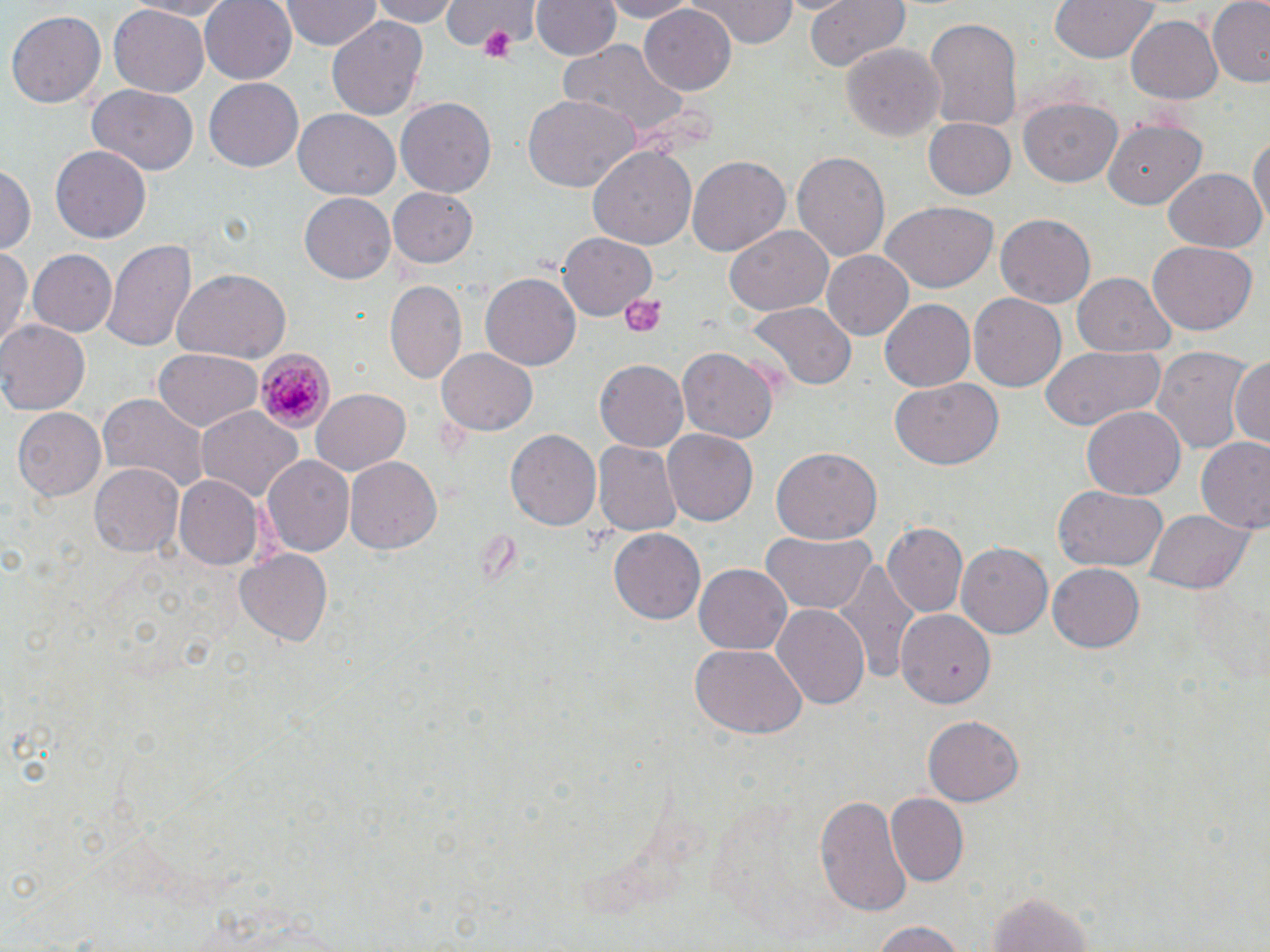
Approximate bounding boxes as (x1,y1)-(x2,y2) corner pairs in pixels. Platelet locations: (477,24)-(518,62), (621,292)-(664,335). Plasmodium malariae-infected red blood cell locations: (258,348)-(334,433). Uninfected red blood cell locations: (125,0)-(241,19), (199,0)-(297,83), (279,0)-(385,53), (369,0)-(456,27), (443,0)-(540,60), (598,0)-(697,21), (689,0)-(795,46), (802,0)-(911,72), (1049,0)-(1161,61), (1206,0)-(1270,85), (532,1)-(619,61), (640,4)-(736,94), (107,7)-(210,95), (6,9)-(107,109), (326,15)-(428,123), (922,16)-(1024,137), (1124,16)-(1224,106), (558,41)-(691,139), (842,42)-(945,143), (202,77)-(304,173), (89,86)-(199,174), (521,92)-(637,192), (1020,95)-(1122,185), (396,96)-(500,197), (291,109)-(399,201), (925,116)-(1015,199), (1101,118)-(1208,209), (1103,121)-(1207,208), (1248,128)-(1269,235), (49,144)-(153,244), (588,146)-(695,254), (792,151)-(889,261), (687,154)-(789,255), (0,163)-(34,256), (1163,167)-(1267,253), (390,189)-(478,268), (299,194)-(395,282), (879,203)-(998,292), (996,214)-(1096,307), (727,227)-(831,314), (558,232)-(657,322), (103,236)-(198,356), (1147,238)-(1255,334), (26,248)-(117,337), (0,250)-(31,355), (821,250)-(913,340), (172,269)-(291,364), (482,273)-(581,371), (1073,273)-(1177,359), (385,280)-(466,382), (968,293)-(1066,393), (879,299)-(975,393), (749,303)-(852,389), (0,320)-(90,415), (1040,344)-(1166,433), (677,345)-(777,441), (1150,346)-(1254,456), (436,348)-(536,436), (151,350)-(261,433), (1231,354)-(1268,453), (594,361)-(689,453), (889,378)-(1004,470), (310,388)-(410,477), (97,394)-(209,492), (1083,406)-(1185,499), (11,407)-(106,502), (195,407)-(302,504), (506,429)-(602,531), (663,430)-(758,526), (1196,439)-(1270,535), (594,440)-(682,537), (771,447)-(882,544), (262,454)-(354,559), (344,457)-(439,555), (88,462)-(184,558), (172,475)-(262,570), (1055,486)-(1167,573), (1143,507)-(1251,595), (884,523)-(968,616), (610,528)-(705,625), (761,531)-(877,615), (957,541)-(1053,639), (236,547)-(336,645), (836,561)-(920,680), (1048,561)-(1147,653), (694,562)-(792,656), (771,604)-(870,710), (896,610)-(994,710), (691,643)-(804,738), (924,716)-(1025,805), (814,792)-(911,917), (885,793)-(969,885), (978,886)-(1099,952), (864,920)-(978,951). Slide-level diagnosis: Plasmodium malariae. Optical microscopy. One field of a larger specimen. Thin blood film. 1000x magnification. Image is 1270×952 pixels. May-Grünwald-Giemsa stain.